Report the malaria status of this cell.
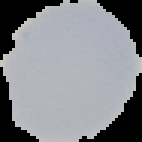

Uninfected.

image type = segmented cell region on a black background
preparation = thin blood smear
image size = 142×142 pixels